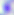
Toxoplasma gondii is seen. 400x magnification. Photomicrograph.